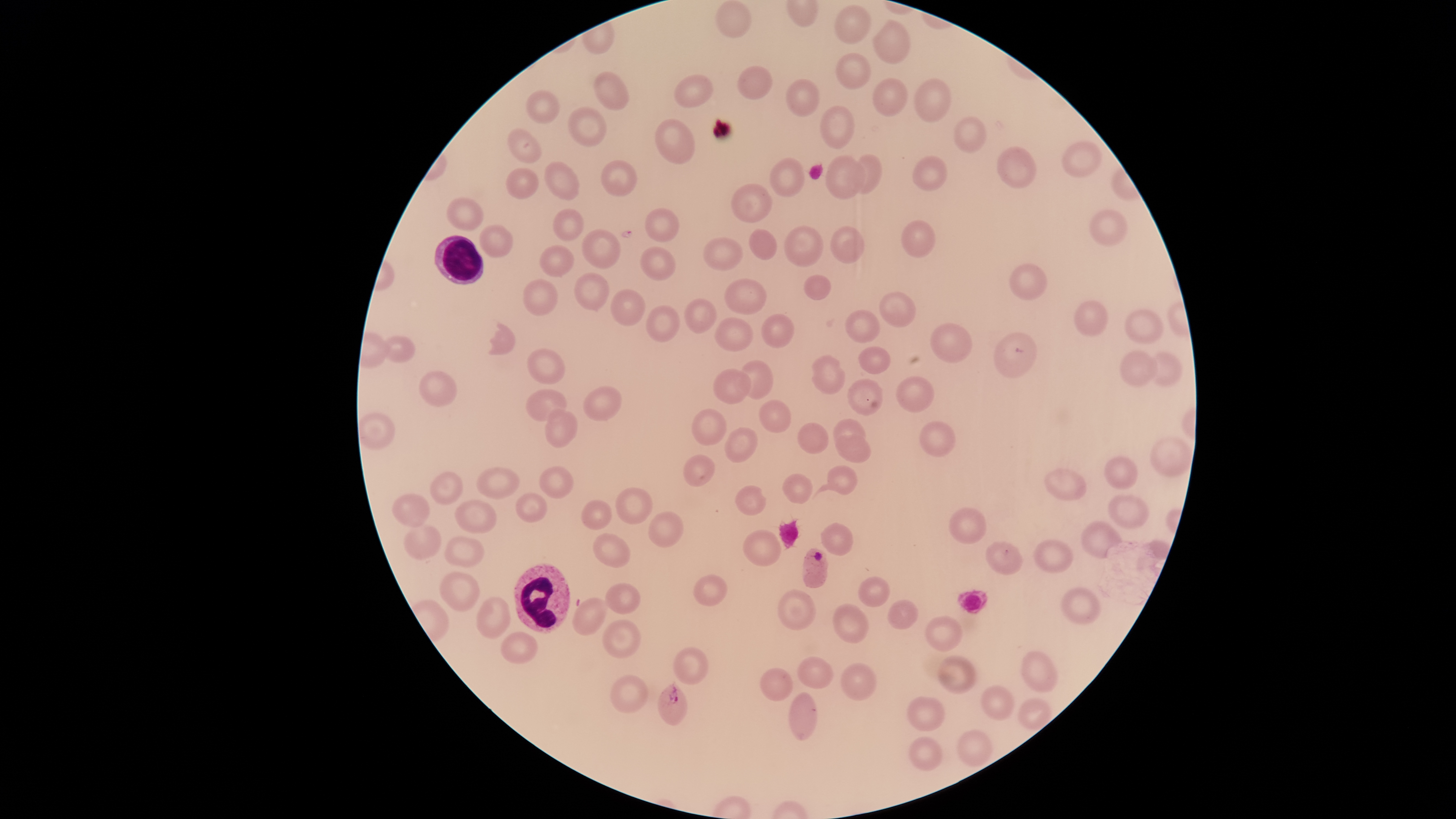

visible_region: circular
WBCs: 'approximate bounding boxes as {left, top, right, bottom} in pixels: {434, 235, 484, 285}, {513, 563, 570, 634}'
species: Plasmodium falciparum
image_size: 1456×819 pixels
preparation: thin blood smear
presence: malaria parasites identified
field_of_view: single
stain: Giemsa
uninfected_RBCs: 'approximate bounding boxes as {left, top, right, bottom} in pixels: {715, 0, 751, 38}, {835, 4, 871, 44}, {873, 19, 911, 64}, {835, 53, 870, 89}, {737, 66, 773, 100}, {593, 71, 629, 109}, {674, 75, 713, 108}, {872, 78, 908, 117}, {914, 78, 951, 123}, {786, 79, 820, 117}, {527, 90, 560, 123}, {819, 105, 854, 149}, {567, 107, 606, 147}, {953, 116, 987, 153}, {655, 118, 695, 164}, {507, 128, 542, 163}, {1061, 141, 1102, 177}, {996, 146, 1037, 188}, {855, 154, 883, 194}, {826, 155, 866, 200}, {912, 155, 947, 191}, {770, 157, 805, 197}, {601, 160, 637, 196}, {544, 161, 580, 201}, {506, 167, 539, 199}, {731, 183, 772, 223}, {446, 197, 484, 231}, {553, 208, 584, 241}, {644, 208, 680, 242}, {1089, 209, 1127, 246}, {900, 220, 936, 258}, {479, 224, 514, 258}, {784, 225, 824, 267}, {830, 226, 865, 264}, {582, 228, 621, 269}, {749, 228, 777, 260}, {703, 237, 743, 272}, {539, 245, 574, 277}, {640, 246, 676, 281}, {1009, 263, 1048, 300}, {574, 272, 610, 311}, {803, 274, 831, 301}, {724, 278, 767, 315}, {523, 279, 559, 316}, {610, 289, 646, 327}, {879, 292, 916, 327}, {684, 298, 717, 334}, {1074, 300, 1109, 336}, {646, 305, 680, 342}, {1124, 308, 1164, 343}, {845, 310, 881, 343}, {761, 313, 795, 349}, {714, 317, 754, 352}, {489, 322, 515, 355}, {929, 323, 972, 363}, {993, 332, 1037, 378}, {383, 335, 415, 363}, {858, 346, 891, 374}, {526, 348, 564, 385}, {1120, 350, 1157, 385}, {1151, 351, 1183, 386}, {811, 354, 845, 394}, {741, 360, 773, 399}, {712, 368, 751, 405}, {418, 370, 457, 407}, {895, 375, 935, 413}, {847, 378, 884, 415}, {583, 386, 622, 421}, {526, 389, 567, 421}, {759, 399, 791, 433}, {544, 409, 578, 448}, {691, 409, 727, 445}, {358, 412, 395, 450}, {833, 418, 866, 445}, {919, 421, 956, 457}, {798, 422, 829, 454}, {725, 427, 758, 462}, {835, 434, 872, 463}, {1150, 436, 1192, 476}, {683, 454, 715, 487}, {1103, 456, 1138, 490}, {814, 465, 858, 497}, {539, 466, 573, 499}, {476, 467, 520, 499}, {1044, 468, 1087, 501}, {430, 471, 464, 505}, {782, 473, 812, 504}, {735, 485, 767, 516}, {615, 487, 653, 525}, {515, 493, 548, 523}, {391, 494, 430, 527}, {1108, 494, 1150, 530}, {454, 499, 497, 533}, {581, 500, 612, 530}, {948, 507, 986, 545}, {648, 511, 684, 548}, {1081, 521, 1122, 559}, {820, 522, 853, 556}, {402, 524, 442, 560}, {742, 529, 782, 567}, {592, 532, 631, 568}, {444, 536, 484, 567}, {1033, 538, 1073, 573}, {985, 540, 1023, 575}, {439, 571, 480, 612}, {693, 574, 728, 607}, {857, 576, 891, 607}, {604, 582, 641, 614}, {1059, 586, 1101, 625}, {777, 589, 817, 631}, {476, 597, 510, 638}, {572, 597, 607, 636}, {887, 598, 919, 630}, {832, 603, 870, 644}, {924, 615, 963, 651}, {601, 619, 642, 658}, {501, 631, 538, 664}, {673, 647, 709, 685}, {1020, 650, 1058, 692}, {937, 655, 978, 693}, {797, 656, 834, 689}, {840, 663, 877, 701}, {760, 668, 793, 701}, {610, 675, 648, 713}, {980, 685, 1014, 720}, {789, 692, 818, 741}, {906, 696, 946, 731}, {1016, 697, 1052, 730}, {956, 729, 991, 767}, {907, 736, 942, 771}'
capture: smartphone photograph through the microscope eyepiece
parasitized_RBCs: 'approximate bounding boxes as {left, top, right, bottom} in pixels: {802, 547, 828, 588}, {657, 682, 688, 726}'